Identify the preparation type.
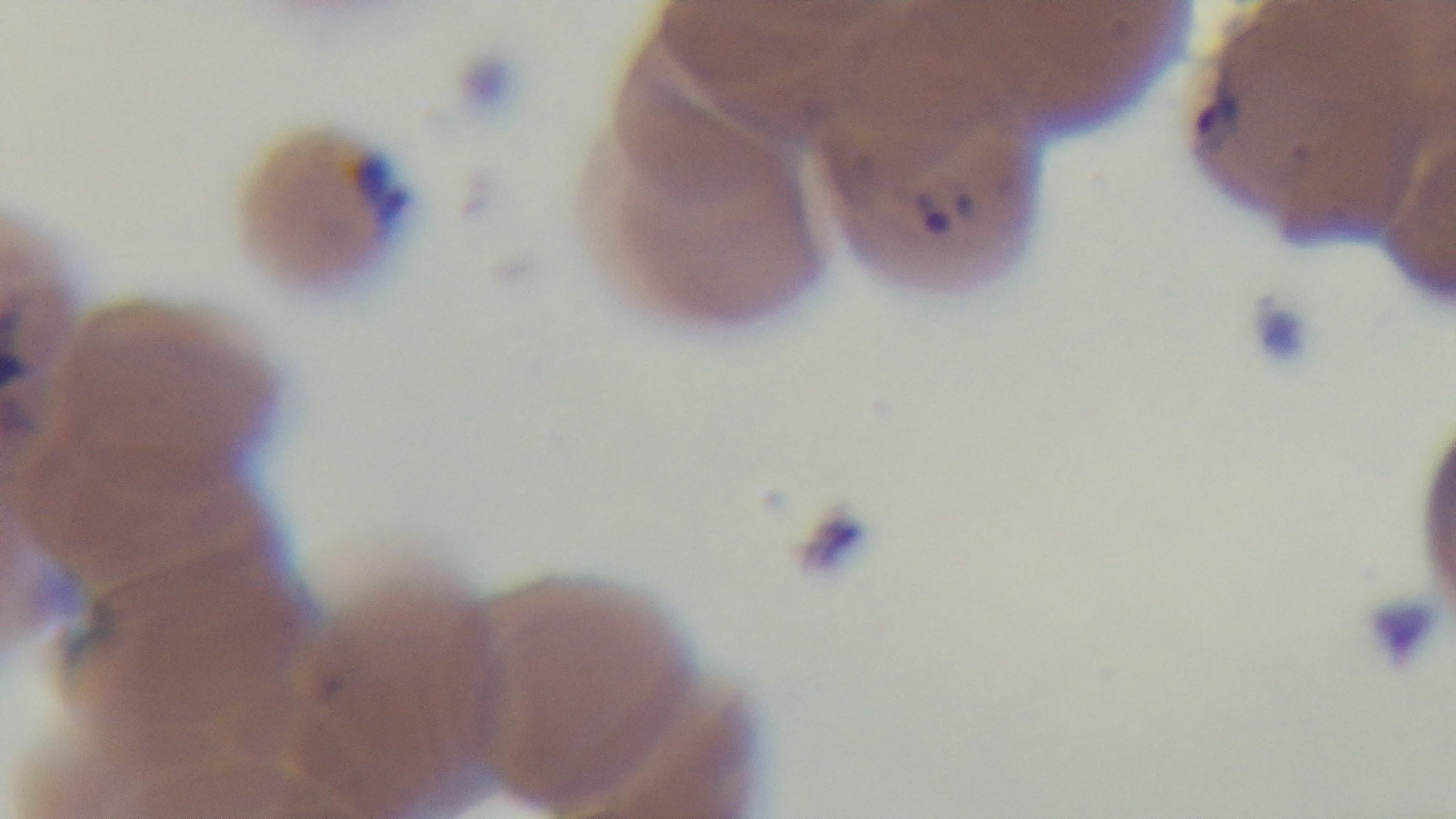
A thin smear.

Summary:
  - Modality: light microscopy
  - Capture: mounted 4K digital camera
  - Objective: 100x oil immersion
  - Malaria status: positive
  - Stain: Giemsa
  - Field of view: one from the slide